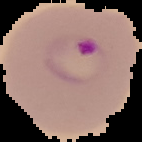

preparation = thin blood film
image size = 142×142 pixels
image type = segmented cell region on a black background
result = malaria parasites detected